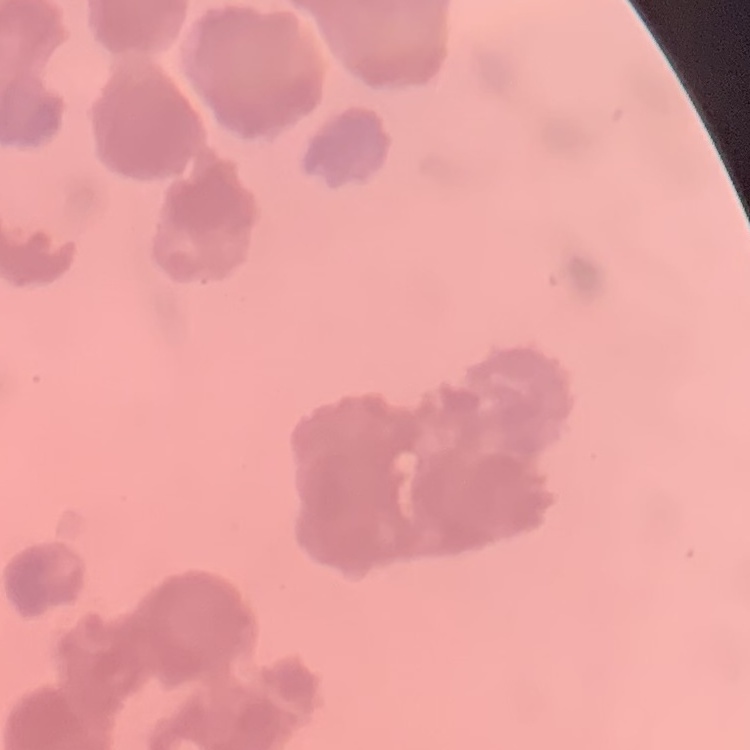

Summary:
  - Erythrocyte morphology: rouleaux formation
  - Stain: Field's or Giemsa
  - Image type: square crop of a larger photomicrograph
  - Preparation: thin blood film